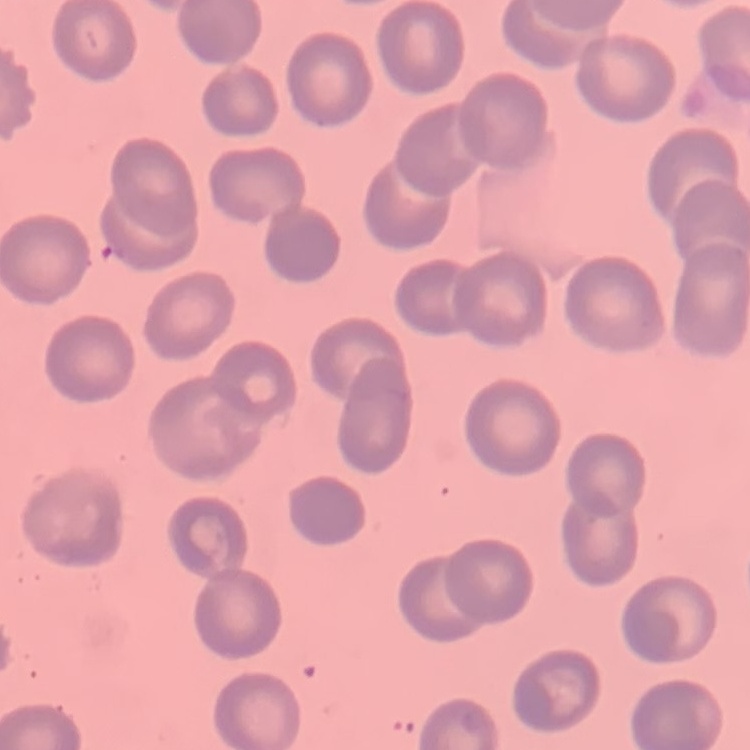

The red blood cells exhibit no rouleaux formation. Field's or Giemsa stain. Thin blood smear. One tile cut from a larger photomicrograph.